State which parasite is depicted.
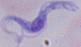

This is a trypanosome.

modality = photomicrograph
magnification = 1000x